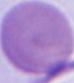

{
  "magnification": "1000x",
  "modality": "photomicrograph",
  "identification": "red blood cell"
}